Point out each malaria parasite.
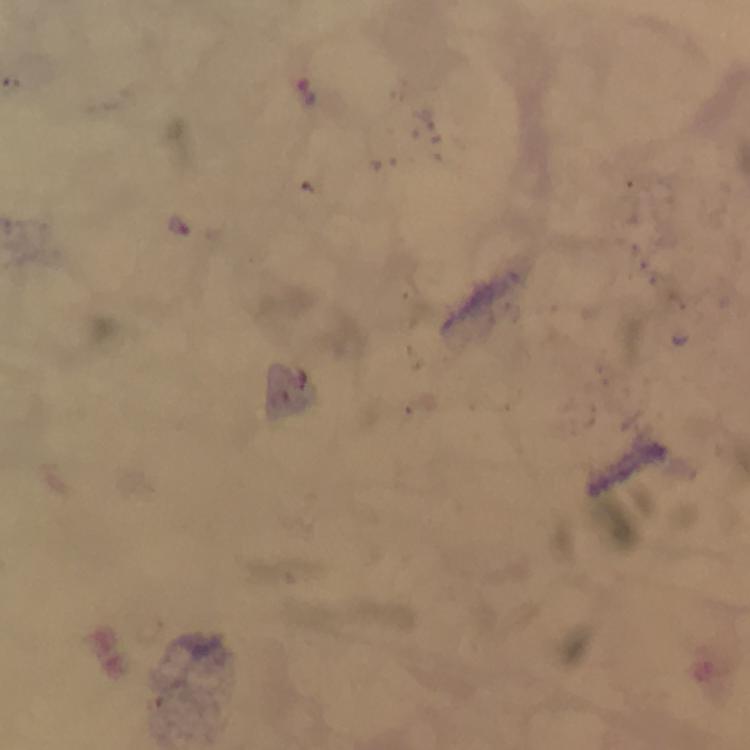
Approximate centers as [x, y] in pixels.
Malaria parasites: [307, 93], [178, 225].

Summary:
  - Capture: smartphone camera through the microscope
  - Immersion oil: applied
  - Magnification: 100x
  - Stain: Giemsa
  - Cropped from: one field of view
  - Image size: 750×750 pixels
  - Preparation: thick blood film
  - Context: from a malaria diagnostic workup